Classify this cell by malaria status.
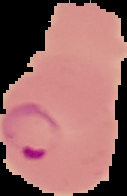
Parasitized.

Summary:
  - Image type: segmented cell region with the area outside set to black
  - Preparation: thin blood film
  - Image size: 127×196 pixels